Give the extent of all Plasmodium falciparum-infected red blood cells.
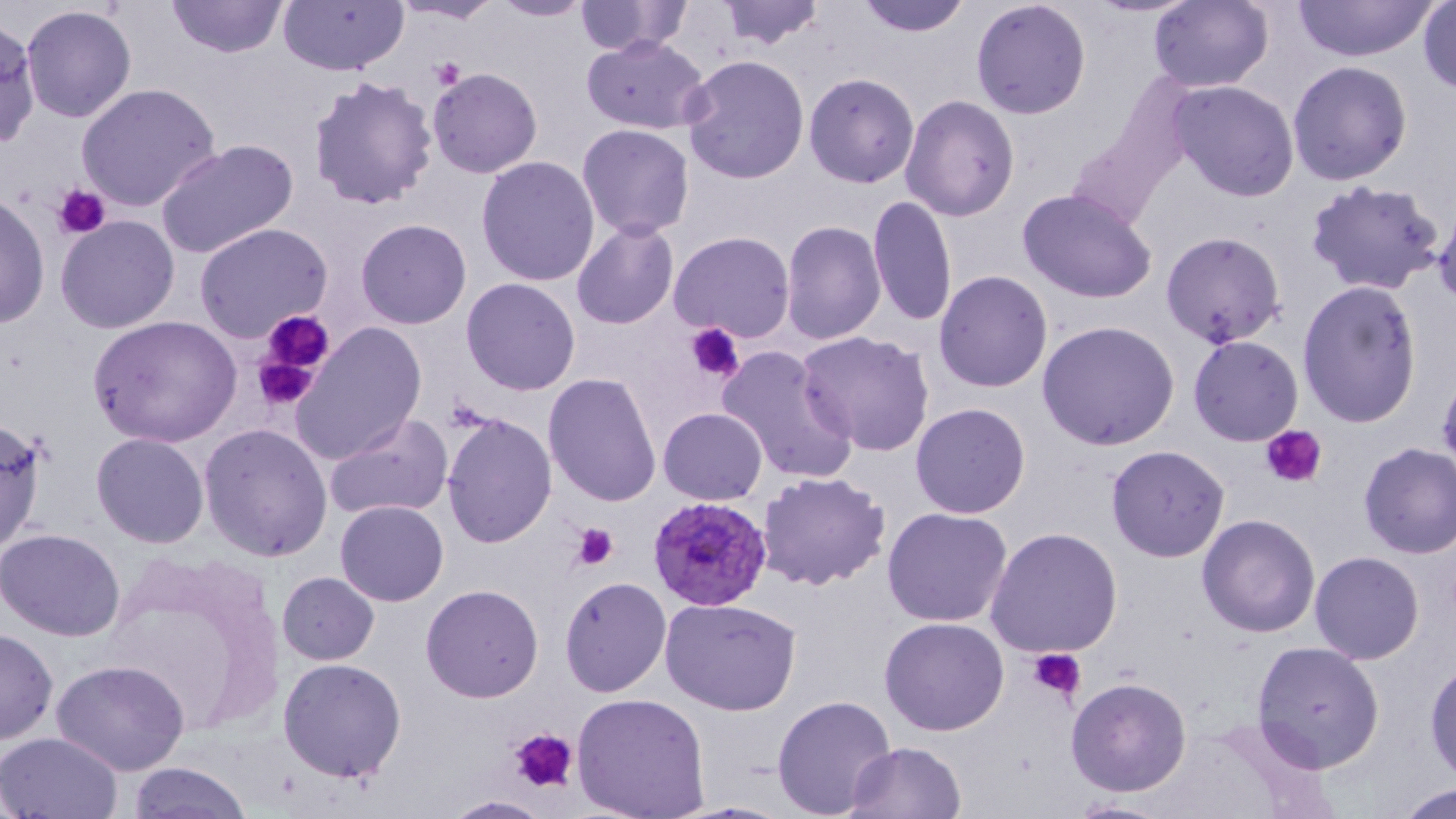
Approximate bounding boxes as [x1, y1, x2, y2] in pixels.
Plasmodium falciparum-infected red blood cells: [646, 495, 774, 612].

{
  "slide_level_diagnosis": "Plasmodium falciparum",
  "platelet_locations": "approximate bounding boxes as [x1, y1, x2, y2] in pixels: [433, 60, 467, 89], [53, 185, 110, 239], [259, 308, 337, 375], [685, 323, 745, 383], [255, 351, 320, 413], [1259, 423, 1328, 489], [569, 523, 619, 571], [1029, 646, 1085, 704], [510, 726, 577, 794]",
  "stain": "May-Grünwald-Giemsa",
  "image_size": "1456×819 pixels",
  "uninfected_red_blood_cell_locations": "approximate bounding boxes as [x1, y1, x2, y2] in pixels: [164, 0, 289, 60], [278, 0, 406, 75], [394, 0, 502, 23], [488, 0, 595, 22], [716, 0, 825, 51], [854, 0, 972, 36], [971, 0, 1091, 119], [1148, 0, 1273, 92], [1290, 0, 1438, 63], [573, 1, 692, 56], [1417, 2, 1455, 95], [21, 5, 136, 124], [0, 17, 41, 155], [581, 35, 710, 132], [680, 55, 809, 184], [1287, 60, 1414, 186], [427, 68, 543, 178], [804, 73, 920, 189], [309, 75, 439, 213], [1166, 80, 1300, 203], [77, 82, 223, 215], [899, 95, 1020, 222], [576, 125, 696, 240], [156, 138, 299, 259], [476, 155, 600, 286], [1303, 179, 1446, 297], [1016, 188, 1159, 307], [1, 193, 49, 330], [868, 194, 957, 328], [56, 215, 180, 334], [356, 218, 471, 329], [781, 219, 885, 345], [572, 220, 678, 330], [194, 223, 333, 343], [668, 231, 796, 344], [1161, 231, 1287, 349], [934, 271, 1052, 392], [461, 278, 581, 397], [1296, 279, 1422, 428], [89, 314, 240, 448], [1036, 319, 1180, 451], [291, 323, 428, 465], [794, 331, 936, 459], [1187, 334, 1304, 447], [715, 345, 859, 485], [544, 371, 664, 507], [910, 402, 1031, 518], [657, 408, 768, 505], [442, 411, 557, 548], [324, 412, 454, 521], [0, 416, 49, 558], [199, 423, 333, 561], [91, 432, 209, 547], [1356, 441, 1455, 560], [1105, 445, 1230, 562], [757, 471, 892, 592], [335, 499, 448, 605], [882, 507, 1014, 626], [1196, 514, 1321, 639], [1, 527, 127, 642], [984, 528, 1124, 657], [1309, 550, 1425, 665], [277, 572, 379, 665], [558, 576, 671, 698], [421, 583, 544, 701], [661, 598, 804, 717], [878, 618, 1009, 736], [1, 629, 58, 744], [1251, 641, 1384, 772], [51, 658, 190, 774], [279, 658, 408, 782], [1425, 659, 1456, 782], [1064, 676, 1193, 797], [571, 692, 711, 818], [770, 695, 897, 819], [1, 732, 124, 819], [843, 741, 968, 819], [128, 760, 252, 818], [1389, 783, 1456, 818], [438, 795, 553, 818], [1061, 798, 1179, 818]",
  "field_of_view": "one of a larger specimen",
  "preparation": "thin blood film",
  "magnification": "1000x",
  "modality": "optical microscopy"
}